Describe the morphology of the erythrocytes.
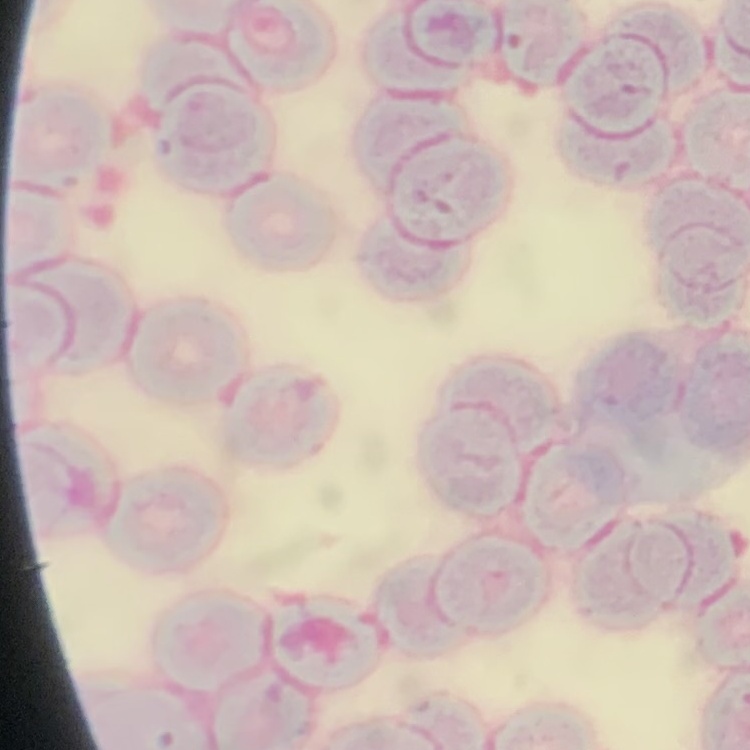

Rouleaux formation.

image type = square crop of a larger photomicrograph
stain = Field's or Giemsa
preparation = thin blood smear